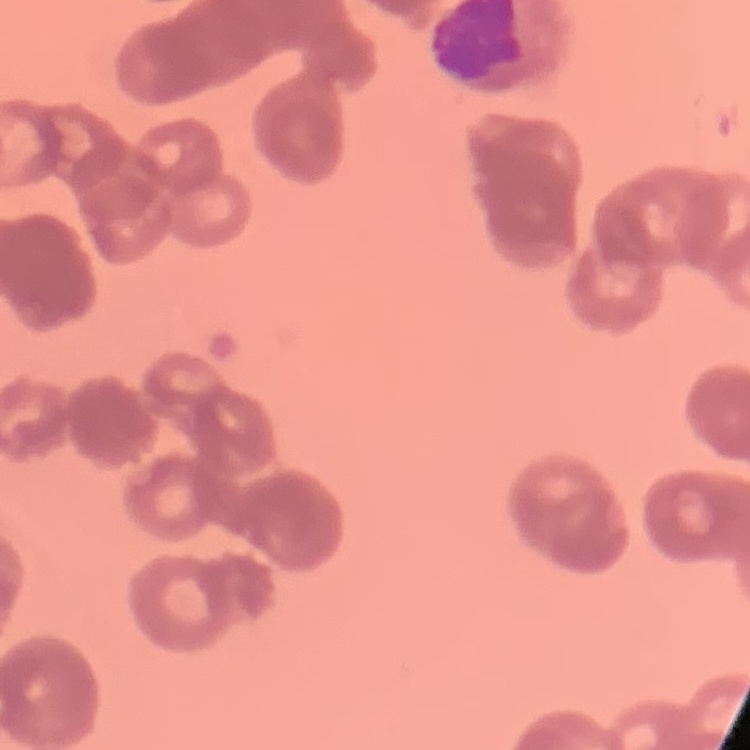

The erythrocytes exhibit rouleaux formation. Thin blood smear. Square crop of a larger photomicrograph. Stained with either Field's or Giemsa.